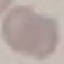

Summary:
  - Malaria status: uninfected
  - Stain: Giemsa
  - Image type: cell patch, automatically extracted from a larger field of view and resized to 64 × 64 pixels
  - Preparation: thin blood smear
  - Capture: smartphone camera at the microscope eyepiece